Locate every blood parasite and identify its species.
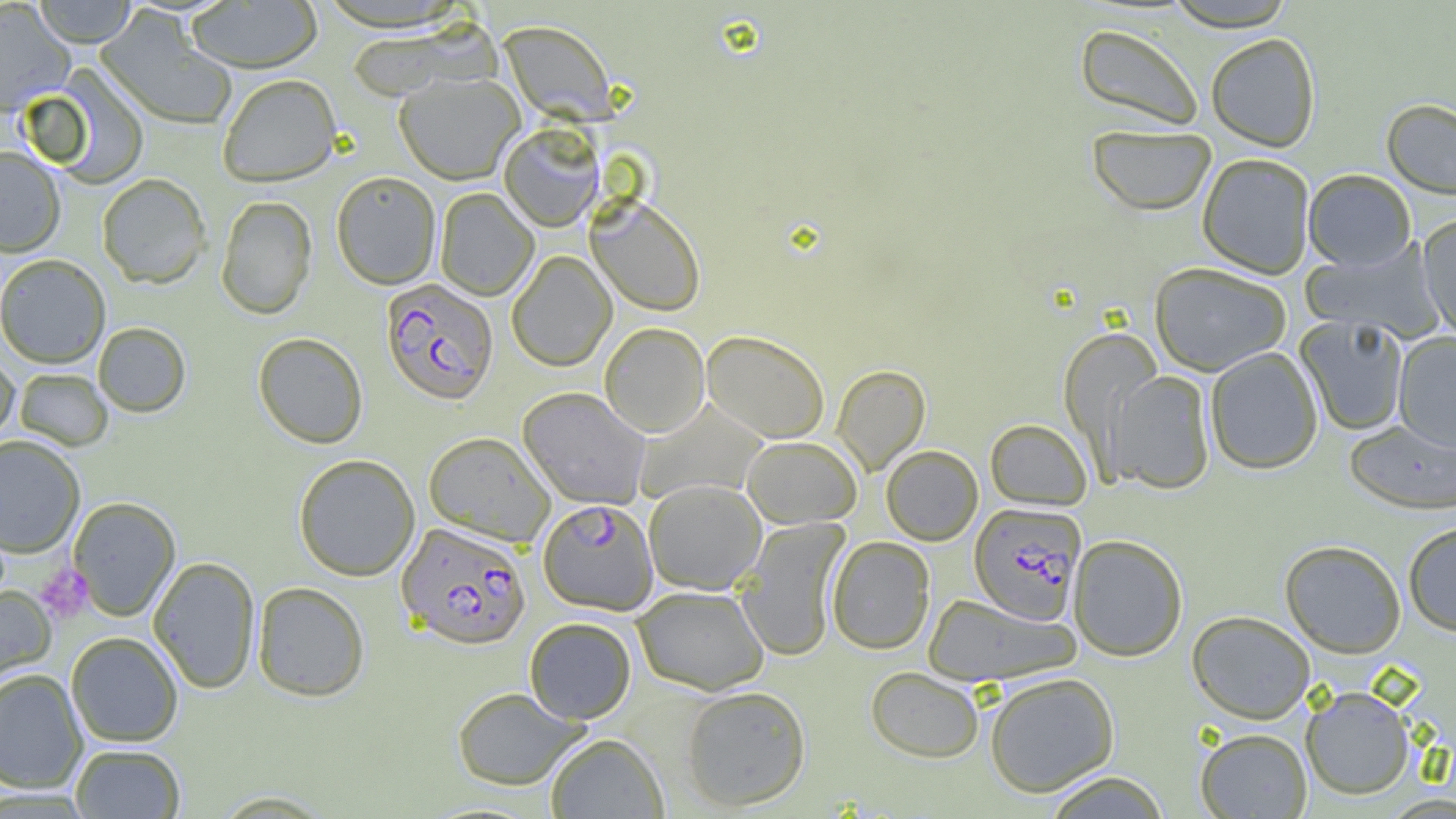
Approximate bounding boxes as (x1,y1)-(x2,y2) corner pairs in pixels.
Plasmodium falciparum-infected red blood cells: (381,280)-(498,405), (538,499)-(658,615), (969,502)-(1086,625), (397,522)-(531,650).
No Plasmodium ovale, Plasmodium malariae, Plasmodium vivax, Babesia divergens, or Trypanosoma brucei observed.

Platelet locations: (36,563)-(93,622). Uninfected red blood cell locations: (33,0)-(137,48), (1162,0)-(1298,31), (0,1)-(75,116), (185,1)-(323,75), (95,9)-(236,132), (499,20)-(619,125), (1074,22)-(1205,132), (1205,32)-(1320,151), (40,66)-(150,189), (394,73)-(524,185), (218,76)-(342,188), (1381,98)-(1456,199), (1087,124)-(1217,216), (499,125)-(604,232), (0,147)-(66,257), (1197,153)-(1315,278), (1303,169)-(1417,271), (331,172)-(441,289), (97,174)-(211,289), (435,188)-(538,301), (216,196)-(317,320), (587,196)-(705,316), (1417,213)-(1456,341), (1301,239)-(1445,342), (507,250)-(616,371), (0,254)-(110,368), (1150,262)-(1291,376), (1295,316)-(1409,436), (600,322)-(710,437), (93,323)-(191,418), (1060,327)-(1164,466), (701,330)-(830,444), (1393,332)-(1456,452), (253,334)-(368,449), (1205,346)-(1323,474), (0,352)-(19,444), (832,365)-(930,475), (14,368)-(113,451), (1106,369)-(1216,494), (518,387)-(650,509), (634,398)-(770,505), (985,419)-(1092,510), (1344,419)-(1456,514), (424,432)-(555,546), (0,435)-(85,557), (742,436)-(862,528), (881,445)-(983,545), (293,454)-(420,581), (643,479)-(766,595), (68,497)-(181,621), (736,516)-(849,662), (1403,521)-(1456,636), (1067,534)-(1188,661), (826,536)-(935,654), (1279,539)-(1407,658), (148,556)-(260,694), (253,582)-(370,702), (0,585)-(56,693), (633,585)-(769,695), (921,593)-(1080,687), (1187,610)-(1316,723), (524,616)-(636,724), (66,631)-(183,747), (865,666)-(984,763), (0,668)-(88,794), (984,672)-(1120,797), (681,685)-(811,812), (1300,685)-(1416,800), (452,687)-(589,792), (1195,728)-(1312,817), (545,733)-(669,819), (70,744)-(186,818), (1041,771)-(1172,818), (210,791)-(337,818), (1380,793)-(1456,819). Slide-level diagnosis: Plasmodium falciparum. Image is 1456×819 pixels. Optical microscopy. Single field of view. Thin blood smear. 1000x magnification.